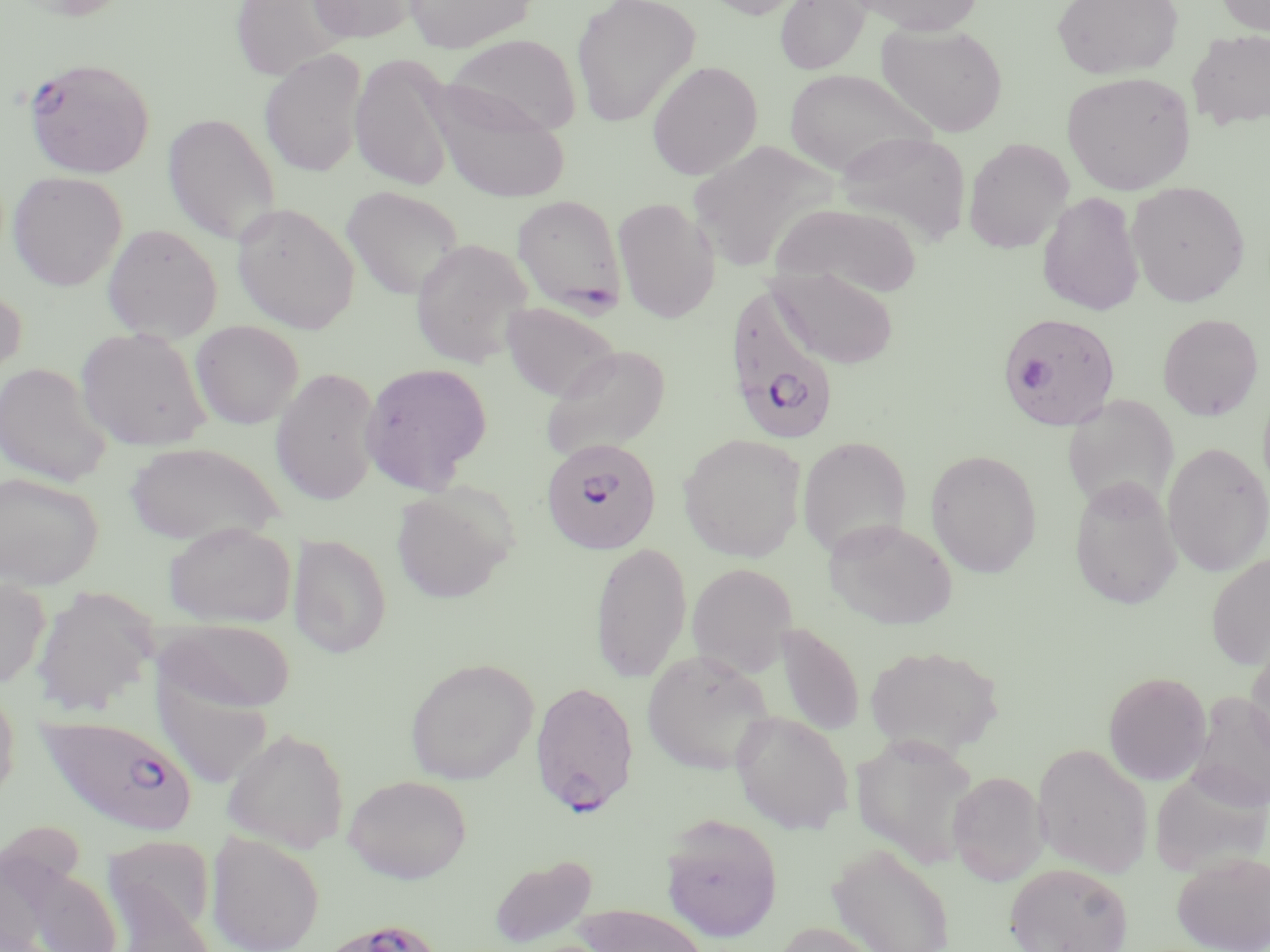
slide-level diagnosis = Plasmodium falciparum
stain = May-Grünwald-Giemsa
modality = light microscopy
preparation = thin blood film
field of view = single
image size = 1270×952 pixels
Plasmodium falciparum-infected red blood cell locations = approximate bounding boxes as (x1, y1, x2, y2) in pixels: (23, 57, 155, 179), (511, 195, 627, 315), (722, 286, 841, 448), (998, 311, 1122, 431), (541, 437, 662, 555), (529, 680, 640, 816), (35, 711, 198, 837), (329, 918, 444, 952)
uninfected red blood cell locations = approximate bounding boxes as (x1, y1, x2, y2) in pixels: (8, 0, 133, 20), (229, 0, 353, 81), (307, 0, 422, 44), (403, 0, 538, 52), (698, 0, 814, 19), (774, 0, 871, 75), (853, 0, 984, 35), (1051, 0, 1184, 80), (1217, 0, 1269, 35), (571, 1, 701, 126), (875, 23, 1008, 137), (1187, 30, 1270, 130), (444, 33, 581, 136), (259, 49, 367, 177), (350, 53, 456, 191), (646, 61, 763, 180), (783, 68, 936, 176), (1062, 71, 1196, 195), (426, 83, 571, 203), (162, 112, 281, 244), (835, 131, 972, 246), (963, 137, 1074, 253), (7, 171, 127, 291), (1127, 180, 1250, 307), (341, 185, 465, 300), (1037, 192, 1144, 316), (612, 197, 720, 323), (231, 202, 360, 334), (772, 202, 923, 298), (101, 223, 223, 343), (410, 238, 533, 369), (770, 267, 899, 369), (0, 286, 28, 389), (500, 302, 623, 402), (1157, 313, 1265, 421), (190, 320, 304, 429), (76, 327, 212, 451), (540, 344, 672, 462), (0, 362, 112, 487), (360, 362, 493, 495), (270, 367, 382, 505), (1061, 394, 1180, 515), (678, 432, 806, 562), (797, 436, 912, 559), (124, 441, 283, 546), (1162, 442, 1270, 576), (925, 449, 1042, 578), (0, 471, 103, 589), (1069, 476, 1183, 610), (390, 486, 513, 604), (824, 519, 957, 630), (163, 522, 296, 628), (288, 534, 392, 659), (589, 542, 691, 683), (1206, 553, 1270, 670), (686, 563, 798, 677), (0, 576, 51, 689), (31, 588, 158, 719), (160, 618, 296, 714), (775, 622, 864, 736), (1245, 640, 1270, 762), (865, 643, 1006, 758), (641, 649, 775, 775), (405, 658, 539, 785), (1103, 671, 1211, 785), (0, 678, 20, 807), (1187, 692, 1270, 811), (730, 711, 854, 834), (222, 728, 350, 853), (851, 733, 980, 868), (1033, 743, 1153, 878), (1149, 767, 1269, 877), (947, 770, 1048, 885), (344, 774, 473, 883), (659, 813, 784, 943), (206, 831, 324, 952), (104, 835, 217, 948), (828, 843, 953, 952), (1173, 850, 1270, 951), (489, 853, 598, 949), (1004, 862, 1134, 952), (22, 866, 124, 952), (574, 904, 712, 952), (773, 921, 889, 952)
magnification = 1000x